Outline each blood parasite and name the species.
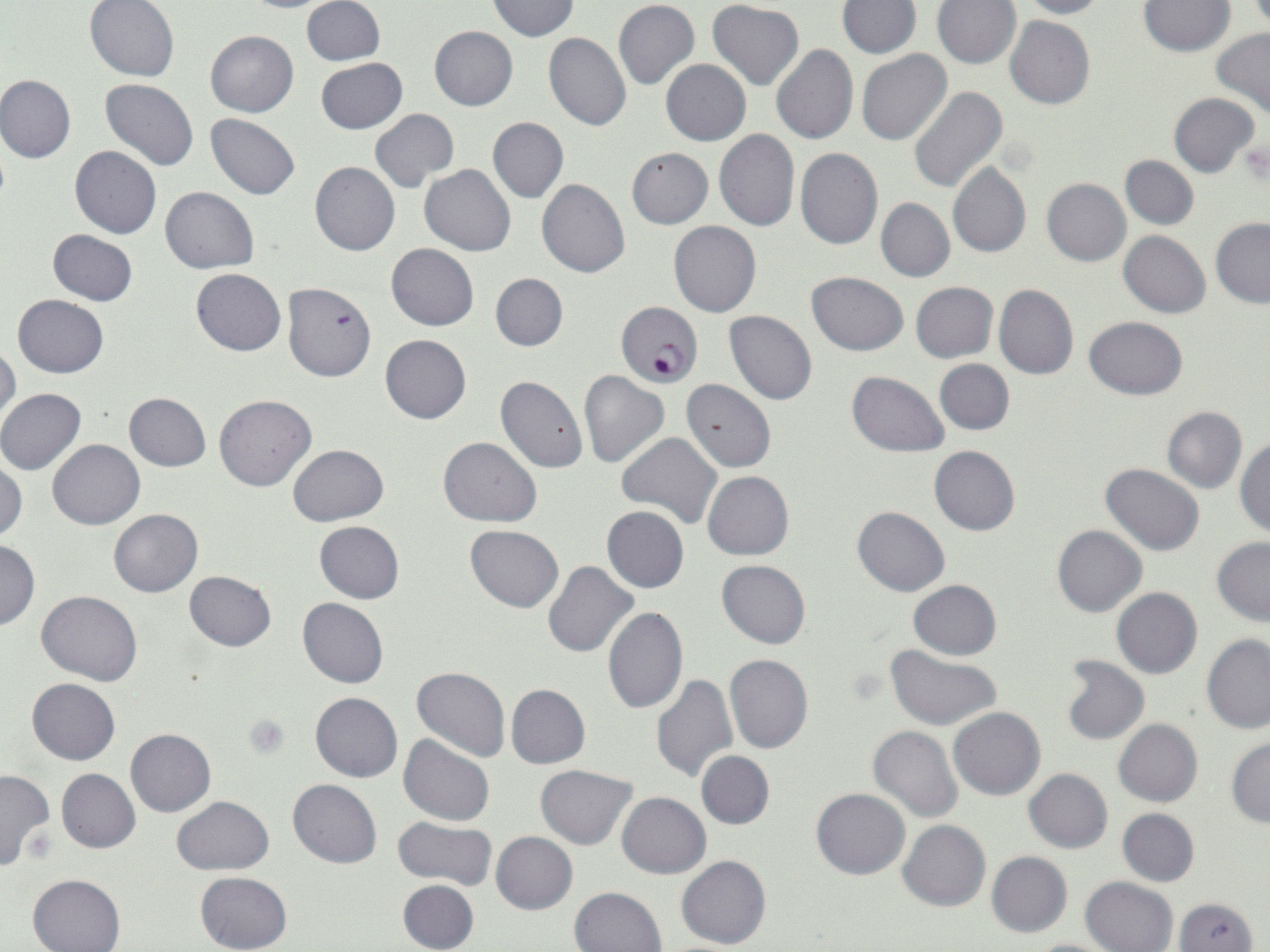
Approximate bounding boxes as (x1,y1)-(x2,y2) corner pairs in pixels.
Plasmodium falciparum-infected red blood cells: (620,303)-(708,389).
No Plasmodium ovale, Plasmodium malariae, Plasmodium vivax, Babesia divergens, or Trypanosoma brucei observed.

Summary:
  - Platelet locations: (1238,138)-(1268,184), (243,713)-(291,760)
  - Uninfected red blood cell locations: (302,0)-(385,67), (487,0)-(579,40), (613,0)-(699,90), (1017,0)-(1106,19), (85,1)-(179,81), (237,1)-(345,13), (708,1)-(804,89), (932,1)-(1020,70), (1139,1)-(1234,56), (836,2)-(920,58), (1006,15)-(1095,108), (429,25)-(518,111), (1211,27)-(1270,120), (205,31)-(298,117), (543,31)-(631,131), (771,44)-(858,145), (857,49)-(951,145), (316,57)-(407,133), (661,59)-(750,145), (0,76)-(76,163), (102,79)-(198,171), (909,86)-(1008,193), (1169,92)-(1259,176), (370,108)-(460,192), (206,114)-(299,199), (488,117)-(568,203), (714,128)-(800,231), (69,145)-(161,239), (627,147)-(713,228), (795,148)-(883,248), (1121,155)-(1198,229), (310,162)-(399,256), (947,163)-(1030,258), (420,165)-(516,256), (1042,178)-(1130,265), (537,179)-(630,277), (161,186)-(258,273), (876,199)-(955,282), (1210,218)-(1270,307), (669,220)-(761,318), (48,229)-(137,305), (1118,230)-(1210,318), (386,243)-(478,330), (191,269)-(286,355), (806,272)-(909,355), (490,273)-(568,351), (911,281)-(999,362), (283,283)-(375,381), (994,283)-(1078,379), (13,295)-(108,377), (725,310)-(816,404), (1084,316)-(1188,400), (380,335)-(471,423), (0,340)-(21,427), (934,358)-(1013,435), (578,370)-(668,467), (846,370)-(948,456), (496,376)-(588,473), (681,379)-(776,472), (0,388)-(86,474), (124,393)-(210,470), (214,394)-(316,491), (1161,406)-(1247,494), (617,432)-(722,529), (438,436)-(541,526), (1235,438)-(1270,536), (49,439)-(143,530), (288,445)-(388,526), (928,445)-(1019,536), (1,458)-(26,541), (1101,464)-(1205,556), (702,471)-(793,561), (602,506)-(689,592), (852,507)-(950,595), (109,509)-(203,597), (315,522)-(404,603), (465,525)-(564,612), (1051,525)-(1146,617), (1211,536)-(1270,625), (0,539)-(38,629), (717,559)-(810,649), (543,560)-(639,658), (184,570)-(276,651), (909,580)-(1001,660), (1111,588)-(1202,678), (38,591)-(142,685), (297,597)-(388,688), (604,606)-(687,715), (1202,634)-(1270,733), (886,648)-(1002,731), (724,653)-(813,753), (1058,655)-(1149,746), (412,666)-(510,762), (651,674)-(737,783), (27,679)-(120,764), (506,684)-(589,768), (310,692)-(402,782), (948,707)-(1044,800), (1113,718)-(1203,806), (868,726)-(962,822), (125,729)-(216,816), (399,735)-(494,826), (1226,738)-(1270,827), (696,751)-(774,828), (536,765)-(637,849), (1023,767)-(1112,853), (0,768)-(55,871), (56,769)-(140,853), (288,779)-(382,868), (811,788)-(909,880), (617,793)-(710,878), (171,797)-(274,875), (1117,808)-(1199,886), (392,816)-(497,890), (898,820)-(990,910), (491,831)-(578,914), (986,851)-(1072,936), (677,855)-(772,949), (194,871)-(292,952), (27,874)-(125,952), (1081,877)-(1178,952), (398,879)-(479,952), (570,886)-(667,952), (1172,895)-(1259,952), (1022,938)-(1122,952)
  - Slide-level diagnosis: Plasmodium falciparum
  - Image size: 1270×952 pixels
  - Preparation: thin blood smear
  - Magnification: 1000x
  - Field of view: single
  - Stain: May-Grünwald-Giemsa
  - Modality: optical microscopy